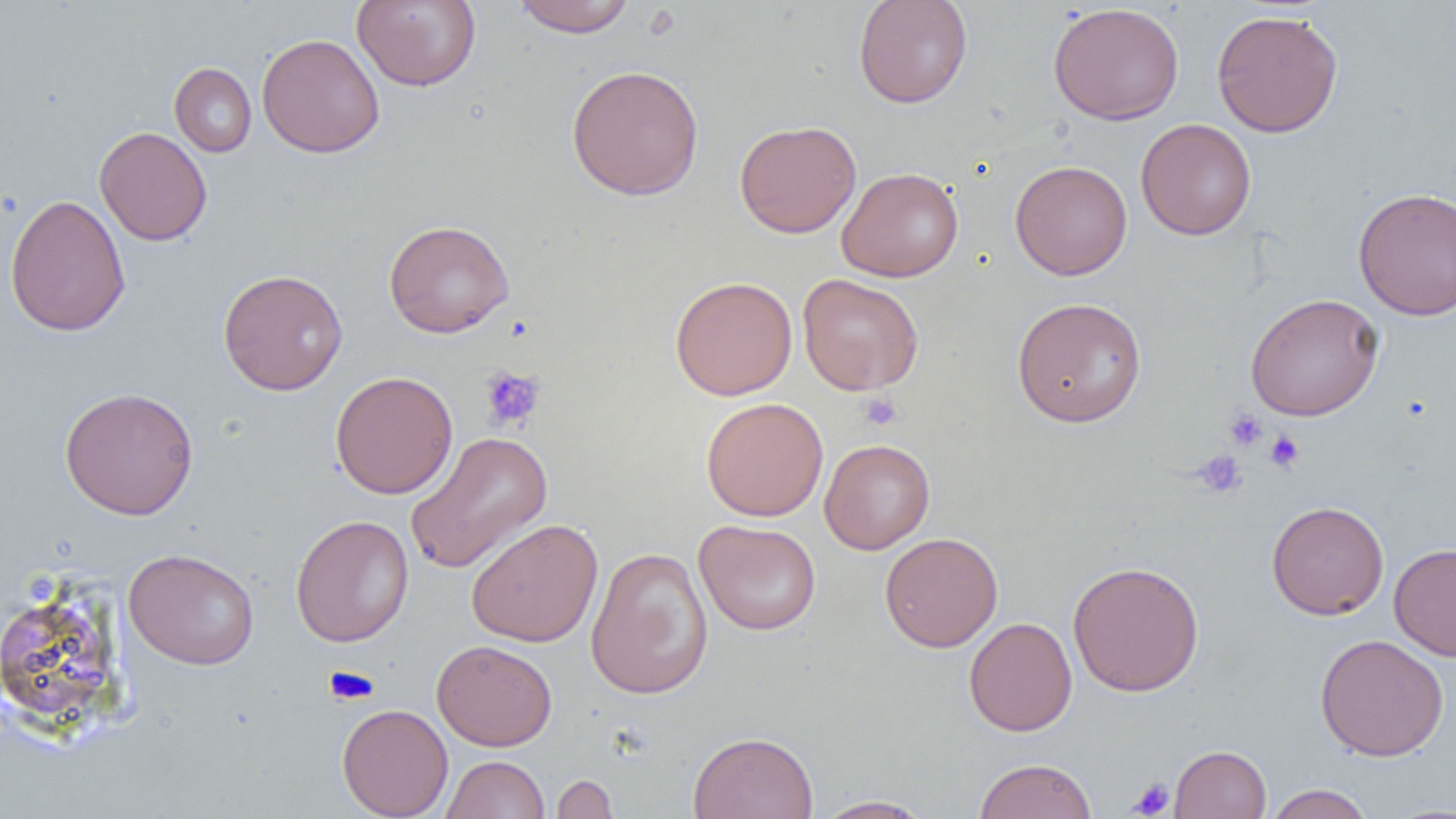
Summary:
  - Coordinate format: approximate bounding boxes as (x1,y1)-(x2,y2) corner pairs in pixels
  - Platelet locations: (480,366)-(546,432), (858,392)-(903,432), (1224,409)-(1267,451), (1265,431)-(1304,472), (1192,450)-(1246,497), (326,666)-(377,704), (1127,778)-(1174,818)
  - Uninfected red blood cell locations: (512,0)-(637,37), (853,0)-(973,109), (351,1)-(481,92), (1047,3)-(1185,126), (1211,9)-(1344,138), (257,33)-(385,158), (169,63)-(257,157), (566,64)-(704,200), (1135,118)-(1256,241), (734,120)-(861,238), (95,126)-(212,246), (1009,160)-(1132,280), (837,166)-(964,282), (1352,187)-(1456,320), (4,194)-(131,337), (383,220)-(514,338), (218,268)-(348,396), (797,273)-(924,395), (669,276)-(798,400), (1245,293)-(1384,421), (1011,296)-(1148,427), (330,371)-(458,499), (60,386)-(199,520), (700,397)-(829,522), (404,431)-(554,575), (819,438)-(935,554), (1266,500)-(1389,620), (290,514)-(414,647), (465,519)-(604,647), (694,519)-(822,636), (879,532)-(1003,652), (1389,542)-(1456,661), (585,545)-(714,700), (123,548)-(260,670), (1067,560)-(1204,698), (1,584)-(127,732), (963,616)-(1077,736), (1315,634)-(1449,761), (432,639)-(558,751), (337,703)-(453,819), (688,730)-(819,819), (1169,745)-(1272,818), (442,755)-(550,819), (974,757)-(1098,819), (550,774)-(619,818), (1264,784)-(1375,819), (812,794)-(935,818), (1377,802)-(1456,818)
  - Slide-level diagnosis: negative for blood parasites
  - Image size: 1456×819 pixels
  - Preparation: thin blood smear
  - Magnification: 1000x
  - Modality: light microscopy
  - Field of view: single